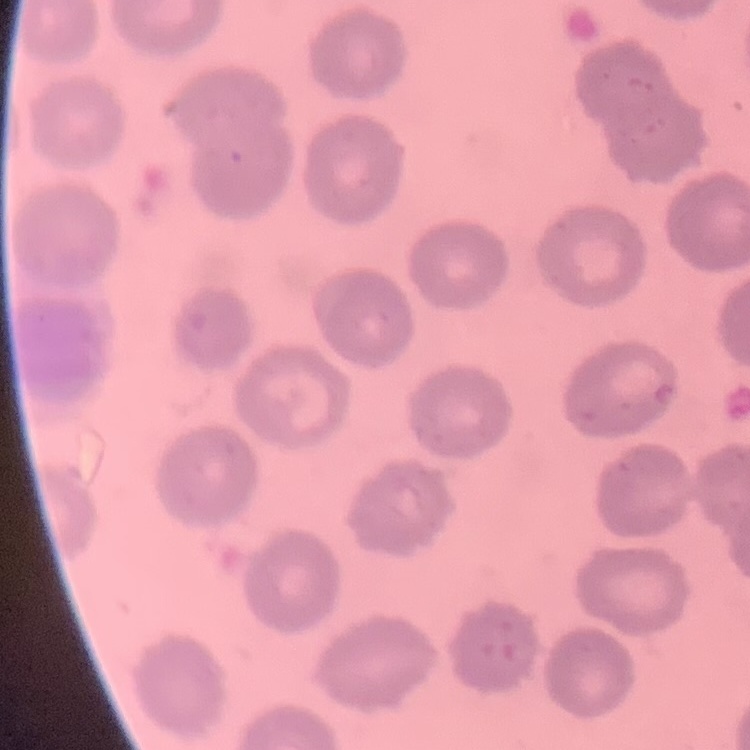

erythrocyte morphology = no rouleaux formation
stain = Field's or Giemsa
image type = square crop of a larger photomicrograph
preparation = thin blood smear